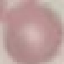
malaria status = uninfected
stain = Giemsa
capture = smartphone through the microscope eyepiece
image type = automatically extracted cell patch, resized to 64 × 64 pixels
preparation = thin blood smear